Name the cell type shown.
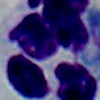

A leukocyte.

magnification = 1000x
modality = micrograph